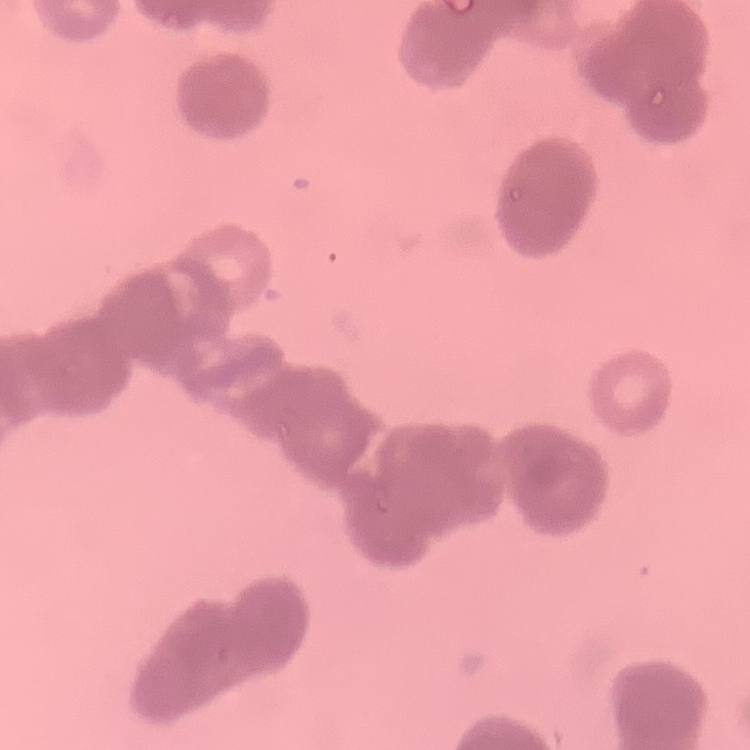
red blood cell morphology = rouleaux formation
image type = square crop of a larger photomicrograph
stain = Field's or Giemsa
preparation = thin blood smear